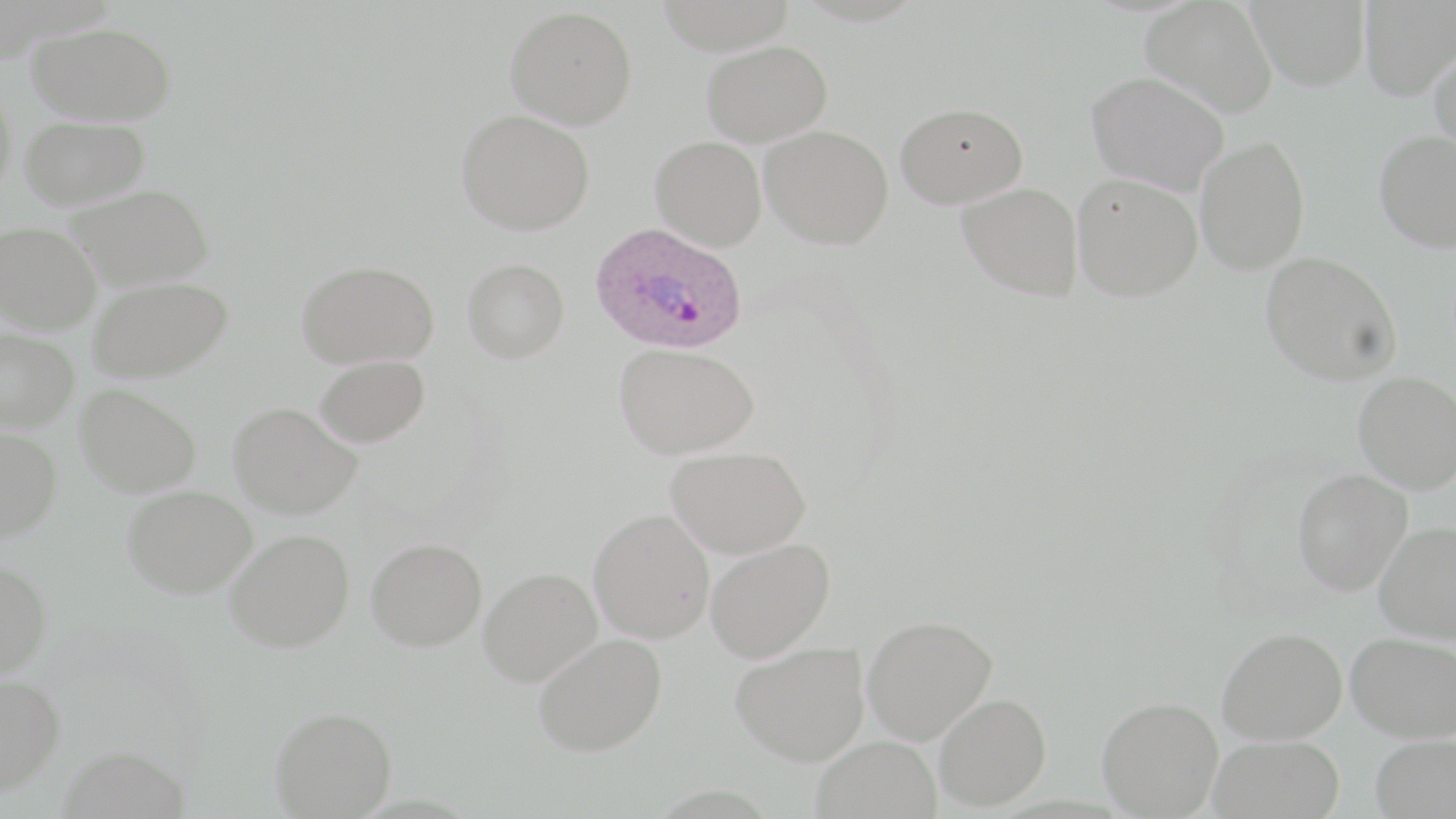
Summary:
  - Coordinate format: approximate bounding boxes as (x1, y1, x2, y2) in pixels
  - Uninfected red blood cell locations: (1141, 0, 1277, 117), (1247, 0, 1371, 90), (1359, 1, 1456, 100), (505, 5, 638, 129), (27, 21, 176, 126), (702, 39, 833, 146), (1429, 42, 1456, 159), (1086, 71, 1229, 195), (0, 85, 17, 197), (895, 102, 1027, 208), (456, 109, 595, 235), (20, 116, 149, 209), (760, 124, 894, 249), (1374, 130, 1456, 252), (1195, 135, 1310, 274), (650, 136, 767, 250), (1072, 173, 1202, 301), (957, 182, 1084, 301), (67, 184, 214, 290), (0, 221, 102, 334), (1260, 250, 1402, 385), (462, 258, 569, 363), (296, 259, 439, 368), (88, 276, 233, 382), (0, 327, 79, 431), (614, 343, 759, 459), (315, 354, 430, 448), (1354, 371, 1456, 493), (75, 384, 203, 497), (227, 401, 361, 520), (0, 427, 62, 542), (666, 446, 811, 558), (1292, 468, 1413, 595), (122, 485, 256, 598), (589, 509, 714, 643), (1375, 521, 1456, 644), (225, 529, 354, 652), (366, 537, 487, 652), (705, 538, 834, 662), (0, 557, 53, 679), (478, 567, 602, 686), (861, 614, 997, 744), (1217, 627, 1347, 744), (1346, 631, 1455, 742), (533, 633, 667, 756), (731, 642, 869, 765), (0, 673, 65, 795), (934, 693, 1050, 811), (1097, 696, 1223, 818), (270, 706, 397, 818), (1370, 734, 1456, 819), (1208, 735, 1345, 819), (811, 736, 942, 819), (57, 743, 190, 819)
  - Plasmodium ovale-infected red blood cell locations: (589, 222, 748, 355)
  - Slide-level diagnosis: Plasmodium ovale
  - Stain: May-Grünwald-Giemsa
  - Image size: 1456×819 pixels
  - Field of view: one of a larger specimen
  - Modality: light microscopy
  - Preparation: thin blood smear
  - Magnification: 1000x